Classify this cell by malaria status.
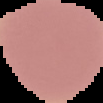

Uninfected.

Summary:
  - Image type: segmented cell region with the area outside set to black
  - Image size: 103×103 pixels
  - Preparation: thin blood film